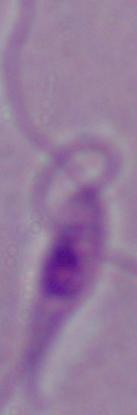
Photomicrograph. A Leishmania parasite is seen. 1000x magnification.